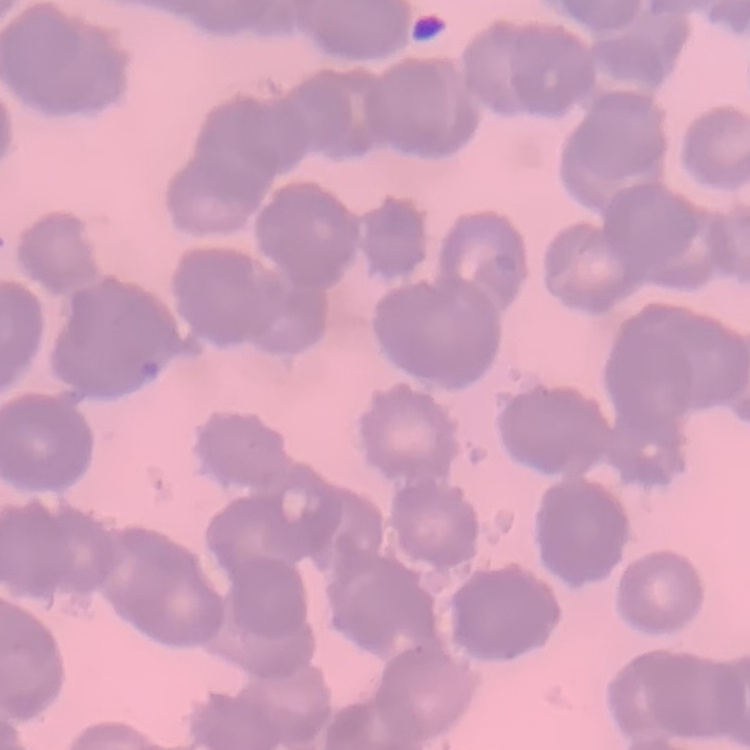
The red blood cells show rouleaux formation. Thin peripheral smear. One tile cut from a larger photomicrograph. Field's or Giemsa stain.